Locate every Plasmodium falciparum-infected red blood cell.
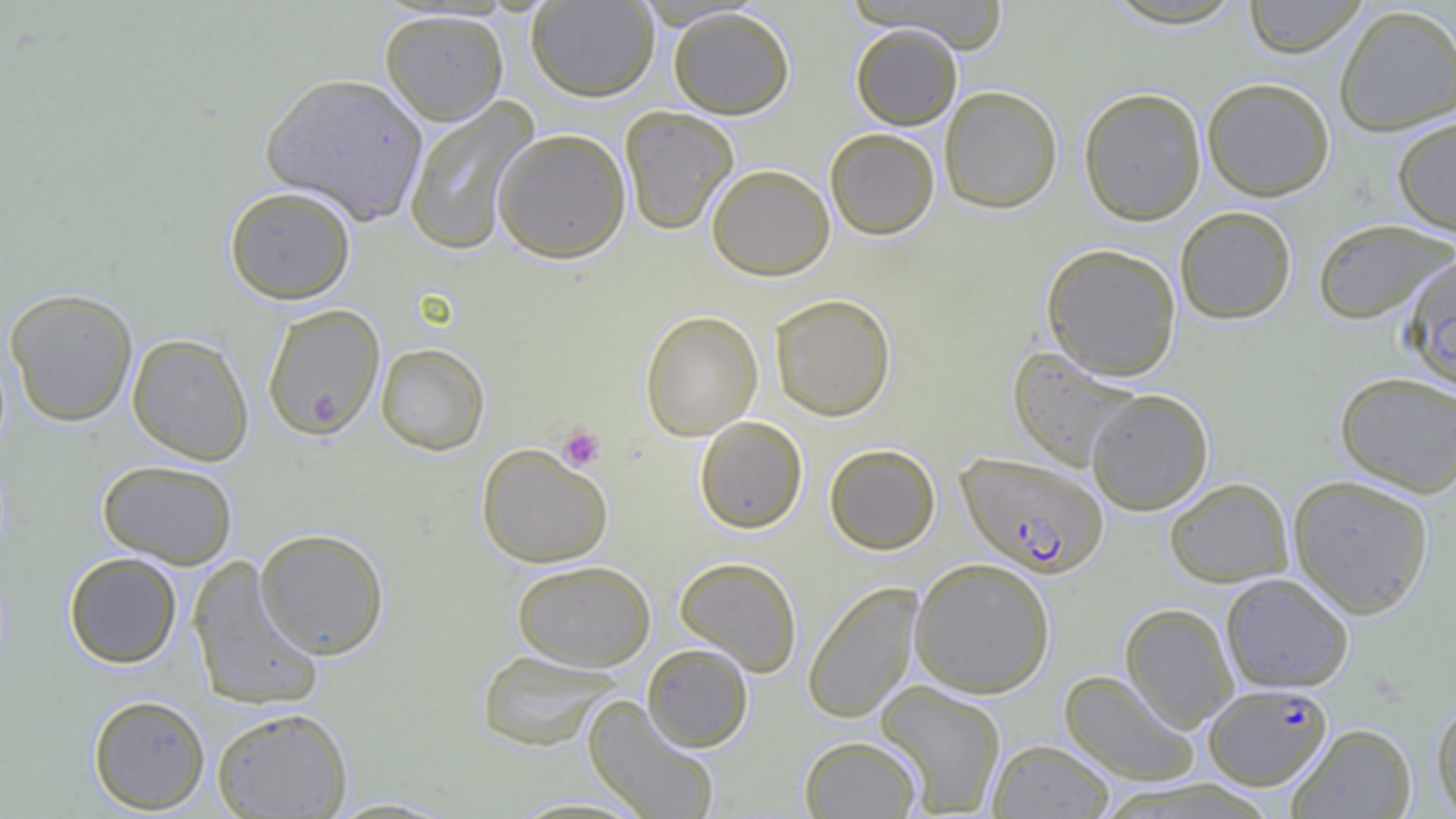
Approximate bounding boxes as [x1, y1, x2, y2] in pixels.
Plasmodium falciparum-infected red blood cells: [957, 452, 1108, 578], [1202, 683, 1333, 790].

{
  "slide_level_diagnosis": "Plasmodium falciparum",
  "platelet_locations": "approximate bounding boxes as [x1, y1, x2, y2] in pixels: [557, 424, 605, 471]",
  "field_of_view": "single",
  "image_size": "1456×819 pixels",
  "preparation": "thin blood smear",
  "magnification": "1000x",
  "modality": "optical microscopy",
  "uninfected_red_blood_cell_locations": "approximate bounding boxes as [x1, y1, x2, y2] in pixels: [526, 0, 660, 102], [1242, 0, 1368, 58], [853, 1, 1013, 53], [1333, 4, 1456, 136], [668, 6, 795, 119], [379, 9, 510, 126], [850, 23, 962, 130], [260, 72, 429, 225], [1201, 77, 1335, 201], [939, 85, 1063, 213], [1078, 87, 1207, 226], [403, 96, 541, 256], [619, 106, 738, 235], [1392, 116, 1456, 237], [493, 127, 631, 264], [824, 127, 940, 240], [707, 163, 835, 281], [224, 186, 356, 305], [1174, 206, 1297, 324], [1312, 218, 1455, 324], [1042, 243, 1182, 381], [1400, 253, 1456, 393], [3, 287, 139, 427], [770, 293, 897, 421], [261, 303, 387, 439], [639, 310, 763, 440], [127, 332, 254, 465], [375, 342, 490, 455], [1006, 346, 1144, 472], [1334, 371, 1456, 497], [1085, 389, 1213, 515], [694, 416, 808, 534], [476, 443, 613, 568], [824, 443, 941, 555], [97, 459, 239, 569], [1287, 474, 1435, 619], [1164, 477, 1294, 587], [254, 527, 390, 660], [63, 551, 183, 669], [186, 556, 325, 712], [675, 556, 803, 676], [909, 557, 1056, 698], [512, 559, 657, 671], [1220, 573, 1354, 693], [802, 581, 924, 723], [1120, 602, 1239, 732], [642, 643, 753, 752], [475, 649, 620, 751], [1059, 669, 1201, 787], [874, 680, 1007, 816], [88, 694, 211, 814], [582, 696, 720, 818], [1431, 696, 1456, 817], [211, 706, 352, 818], [1287, 723, 1417, 818], [799, 735, 922, 818], [987, 739, 1115, 818]"
}